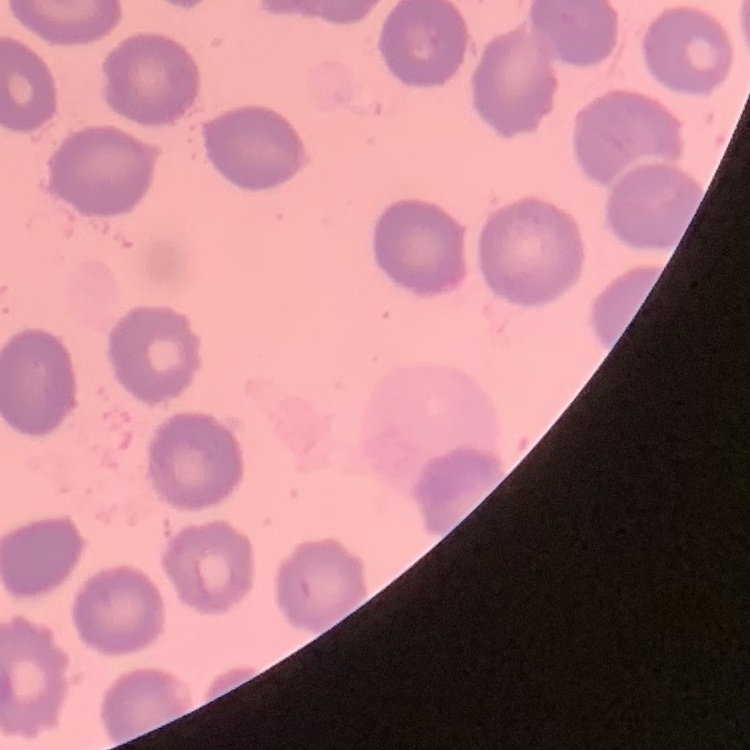
Summary:
  - Red blood cell morphology: no rouleaux formation
  - Image type: square crop of a larger photomicrograph
  - Preparation: thin peripheral smear
  - Stain: Field's or Giemsa